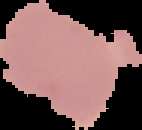 Image is 142×130 pixels. Malaria status: uninfected. From a thin blood smear. Segmented cell region on a black background.